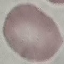

Summary:
  - Malaria status: uninfected
  - Preparation: thin blood film
  - Stain: Giemsa
  - Image type: cell patch, automatically extracted from a larger field of view and resized to 64 × 64 pixels
  - Capture: smartphone camera at the microscope eyepiece